Identify the preparation type.
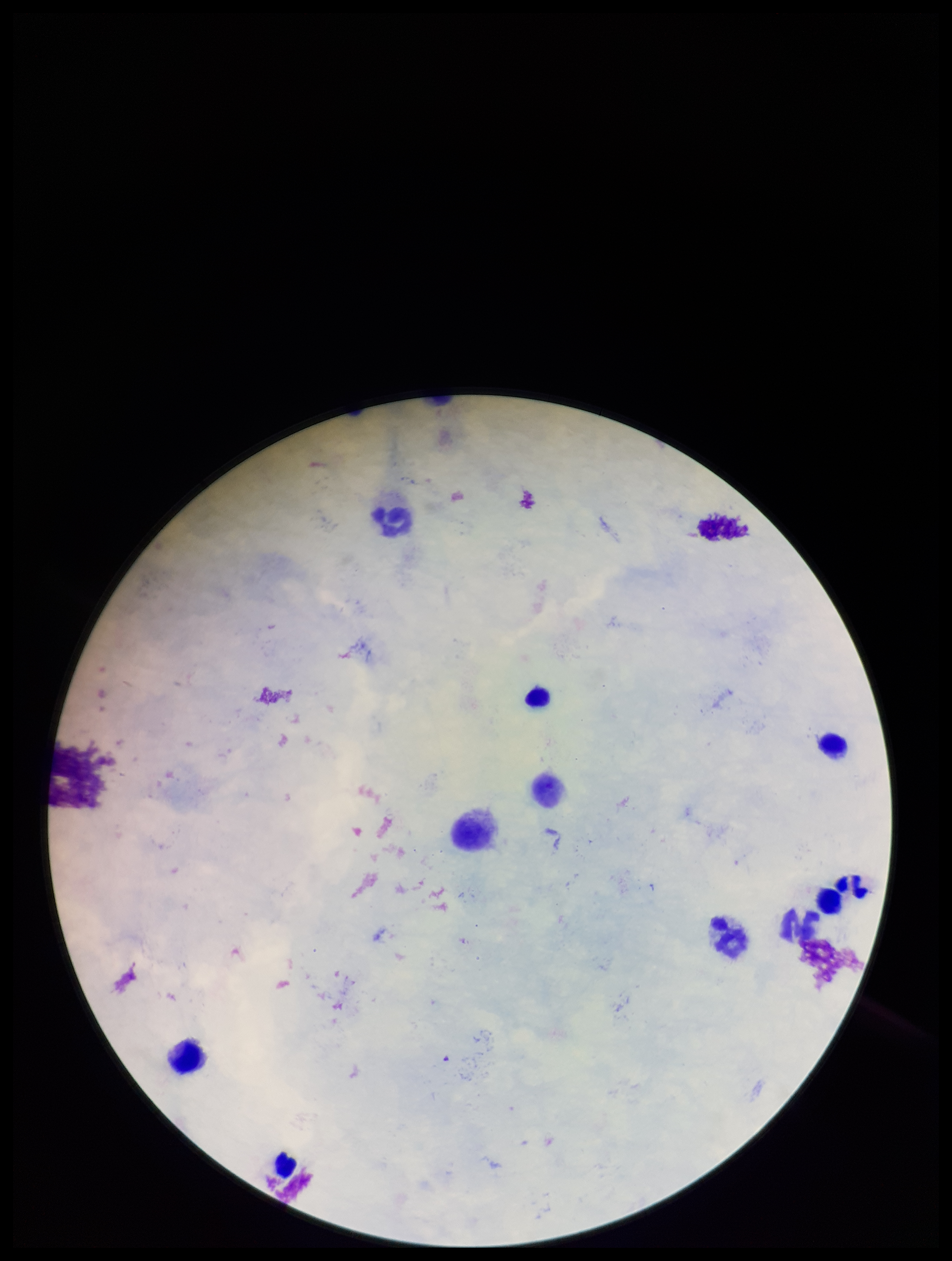
A thick smear.

stain = Giemsa
capture = smartphone photograph through the microscope eyepiece
field of view = one from this slide
parasite count = 0
leukocyte count = 11
Plasmodium parasites = none detected
image size = 952×1261 pixels
patient malaria status = negative